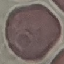
result: no malaria parasites detected
capture: smartphone camera at the microscope eyepiece
stain: Giemsa
image_type: automatically extracted cell patch, resized to 64 × 64 pixels
preparation: thin blood film